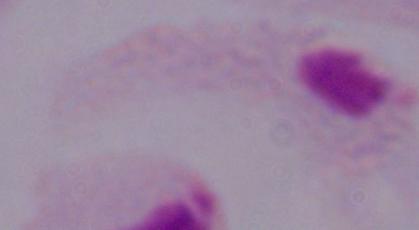

magnification = 1000x
identification = trichomonad
modality = micrograph